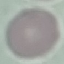
Malaria status: uninfected. Cell patch, automatically extracted from a larger field of view and resized to 64 × 64 pixels. Thin smear of blood. Giemsa-stained preparation. Acquired by smartphone through the microscope eyepiece.